Give the position of every malaria parasite.
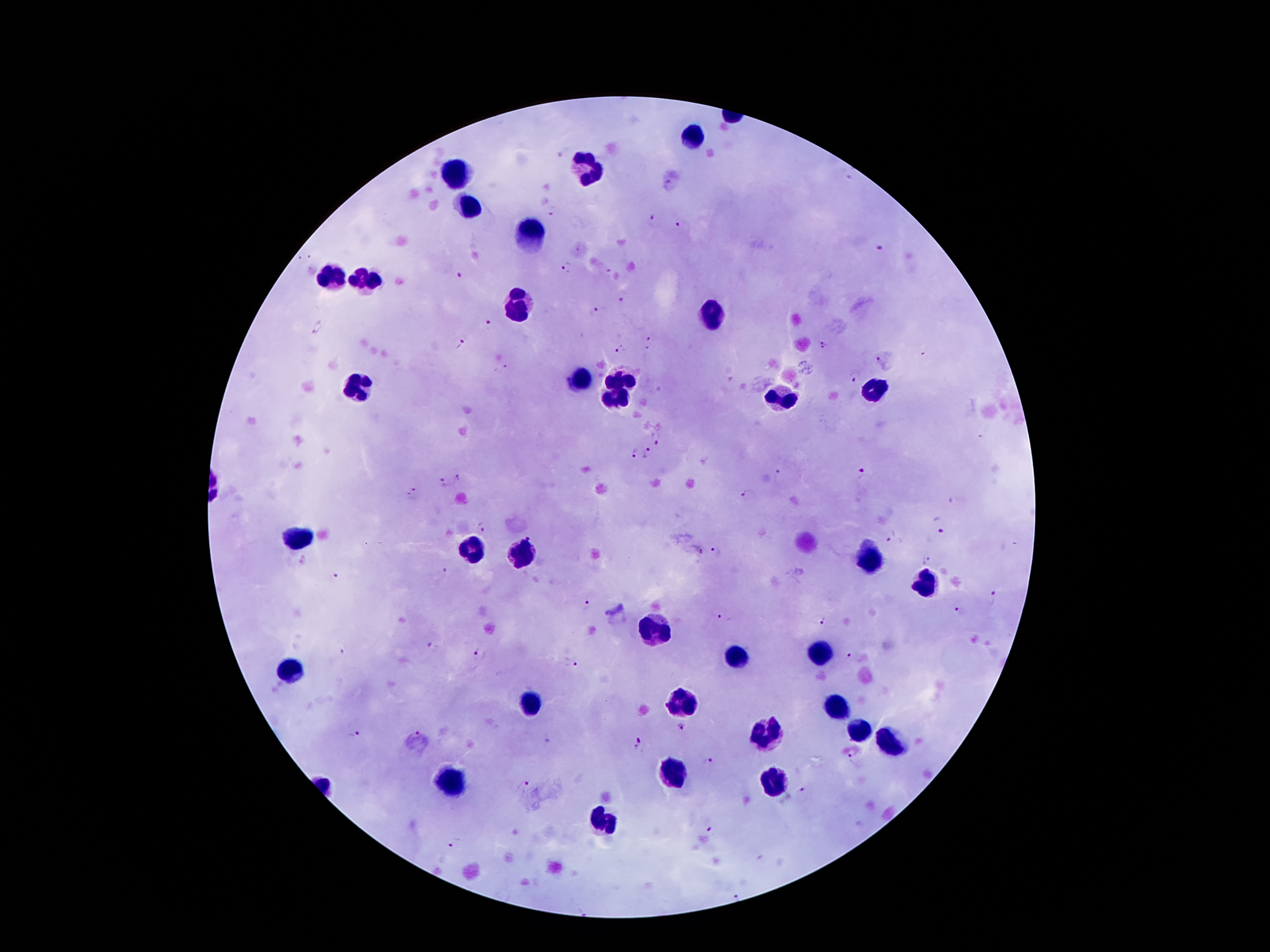

Approximate object centers, in pixels from the top-left corner.
Malaria parasites: (x=564, y=154), (x=553, y=210), (x=652, y=219), (x=679, y=226), (x=882, y=248), (x=568, y=268), (x=460, y=275), (x=623, y=296), (x=600, y=310), (x=491, y=324), (x=318, y=327), (x=650, y=342), (x=462, y=343), (x=823, y=346), (x=621, y=349), (x=877, y=360), (x=506, y=367), (x=855, y=378), (x=658, y=438), (x=649, y=453), (x=635, y=455), (x=781, y=475), (x=861, y=475), (x=462, y=479), (x=444, y=483), (x=749, y=495), (x=413, y=497), (x=483, y=527), (x=943, y=529), (x=888, y=542), (x=701, y=551), (x=717, y=552), (x=927, y=558), (x=445, y=572), (x=334, y=577), (x=995, y=596), (x=586, y=605), (x=960, y=612), (x=723, y=620), (x=817, y=620), (x=434, y=647), (x=341, y=654), (x=481, y=655), (x=853, y=656), (x=569, y=663), (x=681, y=728), (x=355, y=731), (x=414, y=734), (x=549, y=740), (x=640, y=744), (x=851, y=760), (x=708, y=762), (x=523, y=785), (x=803, y=790), (x=713, y=831), (x=455, y=843).

Leukocyte locations: (x=695, y=139), (x=589, y=168), (x=452, y=174), (x=469, y=205), (x=528, y=232), (x=332, y=279), (x=367, y=284), (x=518, y=305), (x=713, y=314), (x=619, y=380), (x=581, y=381), (x=360, y=389), (x=872, y=389), (x=779, y=399), (x=614, y=401), (x=296, y=537), (x=472, y=548), (x=522, y=558), (x=869, y=561), (x=923, y=584), (x=652, y=631), (x=820, y=648), (x=734, y=655), (x=293, y=670), (x=533, y=701), (x=685, y=702), (x=836, y=707), (x=854, y=731), (x=767, y=733), (x=887, y=742), (x=673, y=773), (x=451, y=784), (x=775, y=785), (x=606, y=823). One field from this slide. 100x magnification. Thick blood smear. Patient malaria status: infected with Plasmodium falciparum. Image is 1270×952 pixels. Giemsa stain. Smartphone photograph taken through the microscope eyepiece.